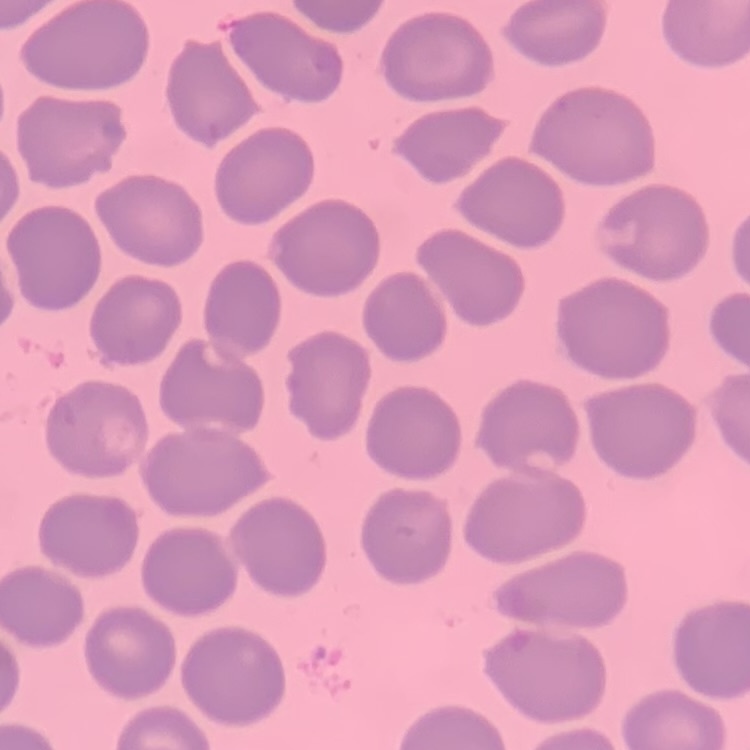

erythrocyte morphology = no rouleaux formation
stain = Field's or Giemsa
image type = one tile cut from a larger photomicrograph
preparation = thin blood film